Give the preparation type.
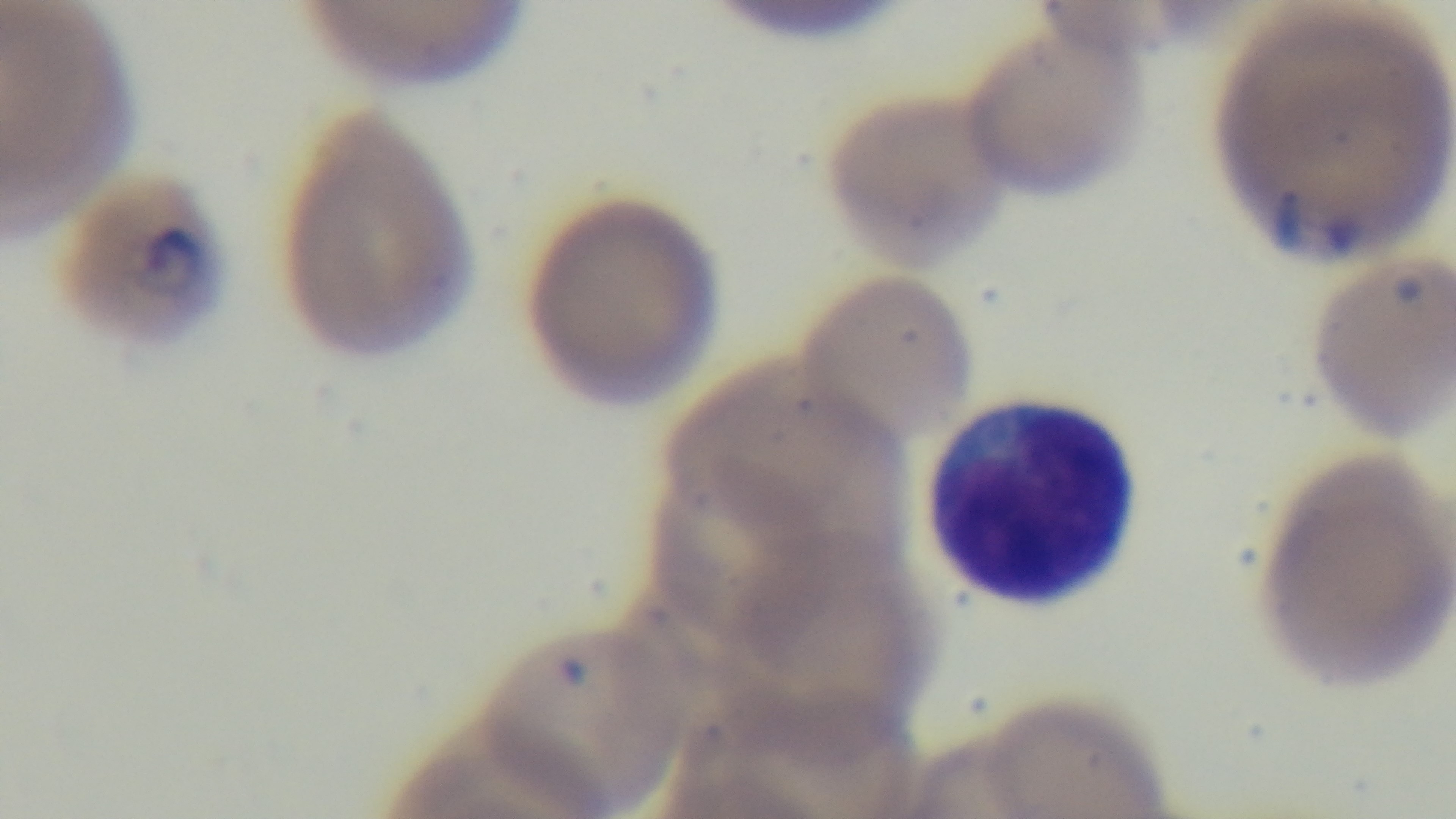
Thin.

Malaria status: positive. Giemsa stain. One field from the slide. Photomicrograph. Captured with a mounted 4K digital camera. 100x oil-immersion objective.